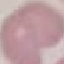

Malaria status: uninfected. Cell patch, automatically extracted from a larger field of view and resized to 64 × 64 pixels. Photographed with a smartphone camera at the microscope eyepiece. Thin smear of blood. Giemsa stain.